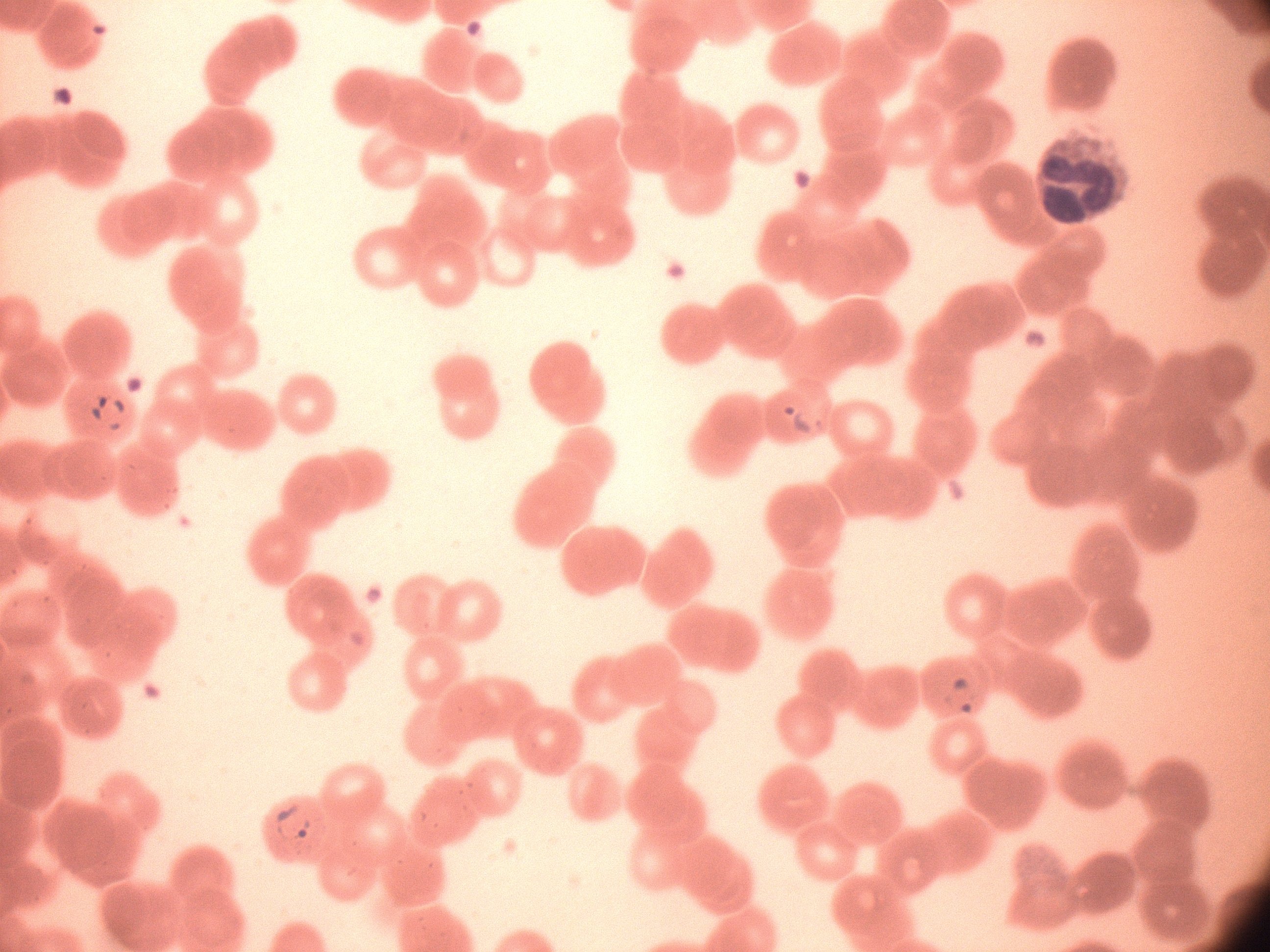

magnification: 100x
field_of_view: single
microscope: Leica DM2000 with built-in camera
preparation: thin blood smear
species: Plasmodium falciparum
stain: Giemsa
image_size: 1270×952 pixels
ring_form_locations: 'approximate bounding boxes as named x1/y1/x2/y2 corners in pixels, from the source annotation, which is not necessarily exhaustive: (x1=87, y1=391, x2=131, y2=434), (x1=780, y1=400, x2=827, y2=437), (x1=940, y1=672, x2=983, y2=720), (x1=269, y1=801, x2=318, y2=848)'